Name the parasite shown.
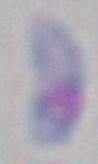

Toxoplasma gondii.

Summary:
  - Magnification: 1000x
  - Modality: photomicrograph